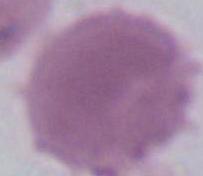

magnification: 1000x
identification: erythrocyte
modality: micrograph